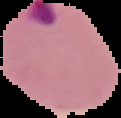
Result: Plasmodium parasites detected. Image is 121×118 pixels. From a thin blood smear. The area outside the segmented cell region is set to black.